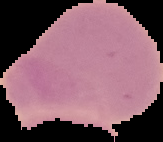

{
  "image_size": "163×142 pixels",
  "preparation": "thin blood film",
  "result": "no Plasmodium parasites detected",
  "image_type": "segmented cell region on a black background"
}